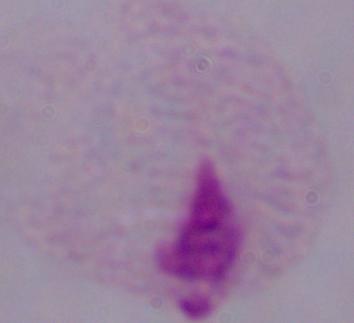
Summary:
  - Magnification: 1000x
  - Modality: photomicrograph
  - Identification: trichomonad